Classify this cell by malaria status.
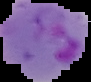
It is parasitized.

image size = 91×82 pixels
preparation = thin blood smear
image type = cell region segmented out of the field of view; surrounding area masked to black